Point out each Plasmodium parasite.
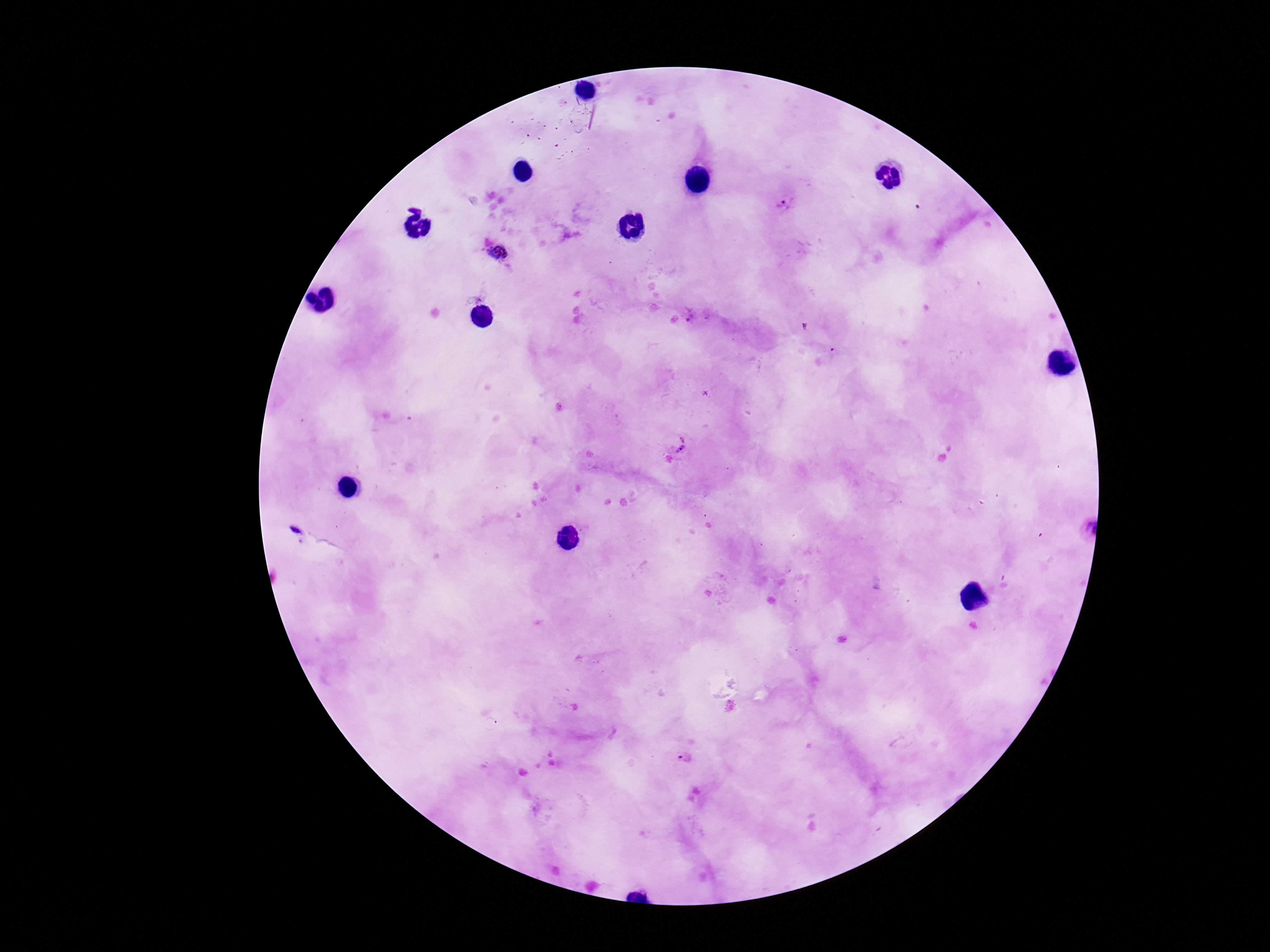
Approximate centers as [x, y] in pixels.
Plasmodium parasites: [782, 205], [499, 252], [678, 446], [684, 759].

Patient malaria status: infected. Image is 1270×952 pixels. Photographed through the microscope eyepiece with a smartphone camera. 100x magnification. Single field of view. Giemsa-stained preparation. Thick blood smear.